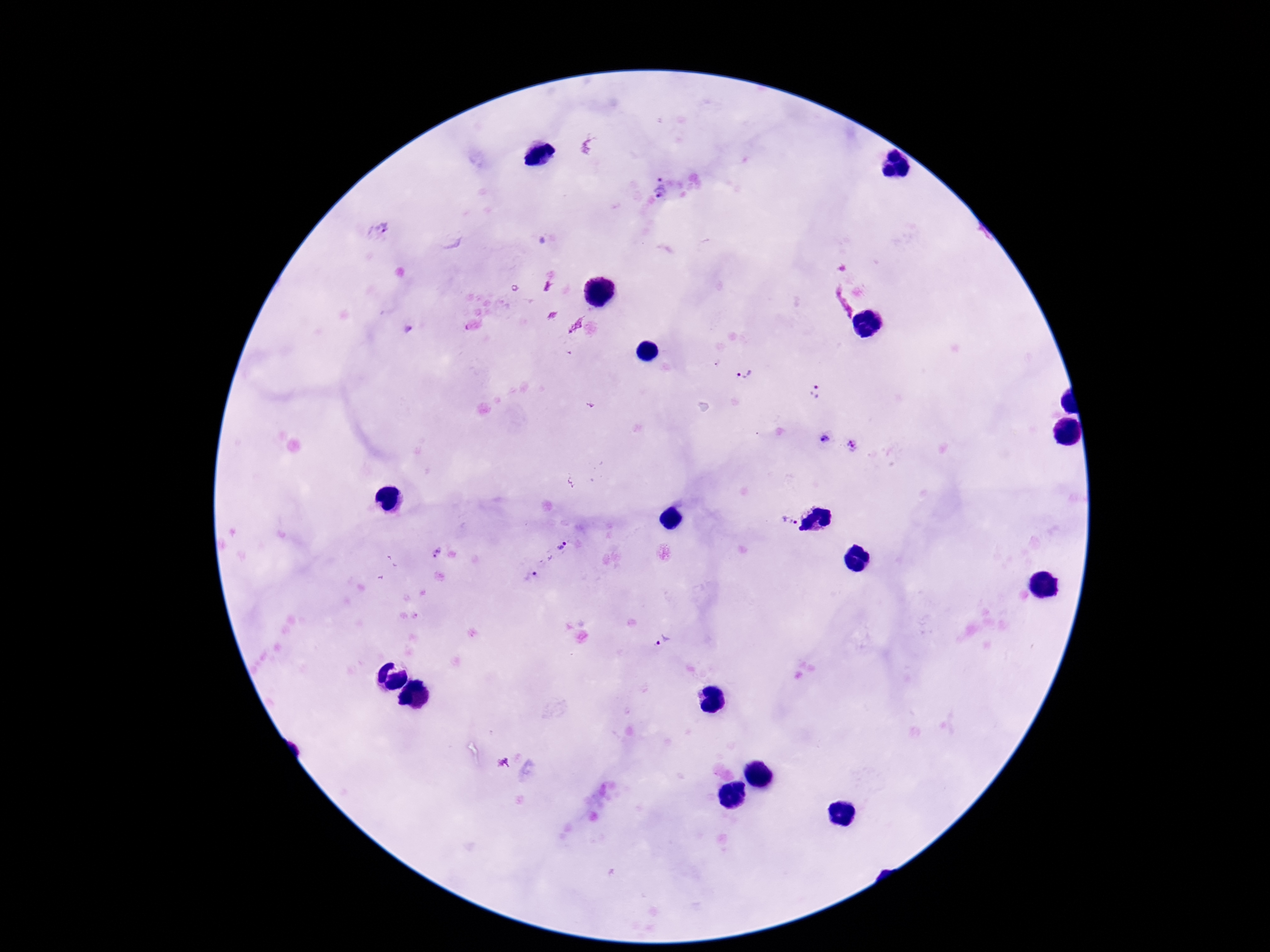
Approximate centers as {x, y} in pixels. Plasmodium parasite locations: {660, 186}, {379, 230}, {473, 326}, {408, 330}, {743, 372}, {815, 392}, {824, 439}, {851, 445}, {784, 521}, {560, 548}, {435, 552}, {531, 574}, {661, 641}, {502, 763}. Single field of view. Smartphone photograph taken through the microscope eyepiece. Thick blood film. Patient malaria status: infected. Giemsa-stained preparation. Image is 1270×952 pixels. 100x magnification.